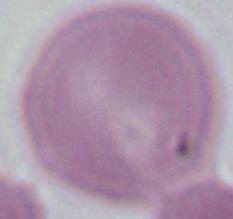

Summary:
  - Modality: micrograph
  - Magnification: 1000x
  - Identification: erythrocyte